Assess the morphology of the red blood cells.
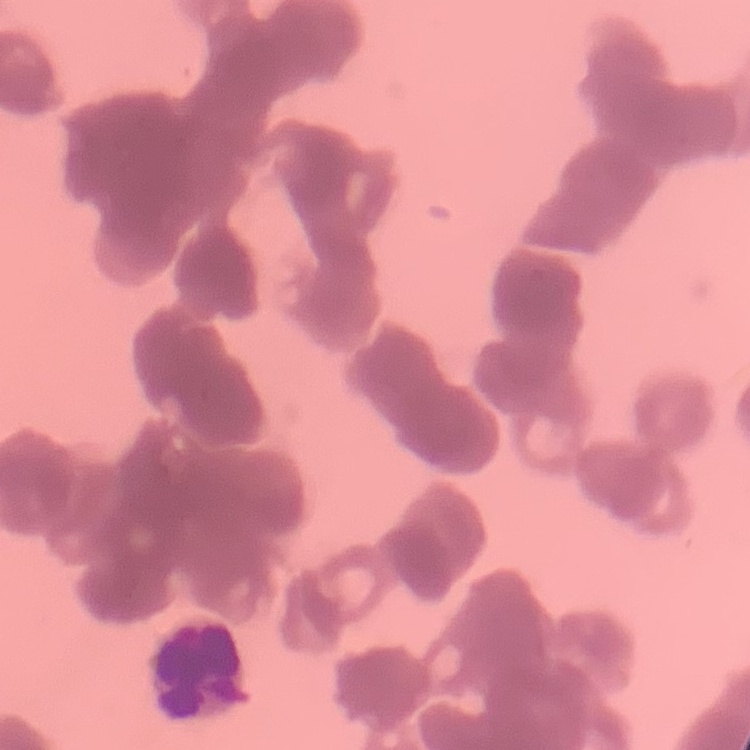
They show rouleaux formation.

Field's or Giemsa stain. Thin peripheral smear. One tile cut from a larger photomicrograph.